Assess this cell for malaria.
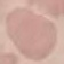

It is uninfected.

preparation = thin blood film
capture = smartphone through the microscope eyepiece
image type = cell patch, automatically extracted from a larger field of view and resized to 64 × 64 pixels
stain = Giemsa